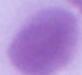

A red blood cell is seen. Captured at 1000x magnification. Photomicrograph.